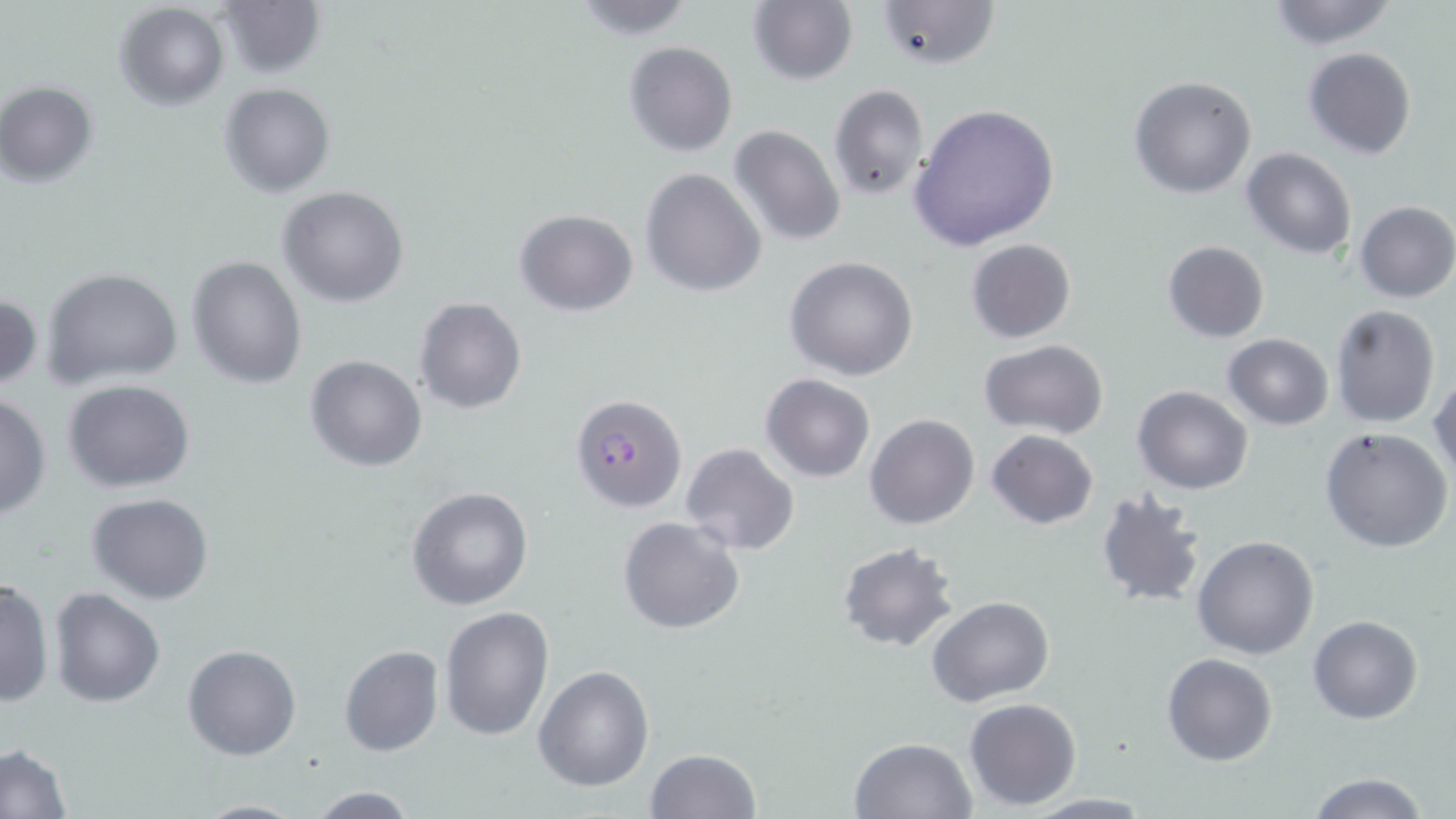

Summary:
  - Coordinate format: approximate bounding boxes as [x1, y1, x2, y2] in pixels
  - Plasmodium falciparum-infected red blood cell locations: [570, 393, 687, 514]
  - Uninfected red blood cell locations: [566, 0, 699, 40], [748, 0, 858, 85], [872, 0, 998, 70], [1261, 0, 1401, 50], [215, 2, 324, 78], [114, 3, 229, 111], [623, 41, 738, 157], [1301, 47, 1417, 160], [1129, 74, 1258, 198], [1, 80, 98, 186], [219, 82, 336, 198], [828, 84, 930, 201], [907, 103, 1061, 251], [728, 125, 847, 247], [1241, 147, 1357, 259], [640, 168, 766, 297], [277, 185, 409, 308], [1355, 200, 1455, 302], [514, 209, 638, 314], [966, 238, 1076, 343], [1162, 240, 1270, 342], [785, 255, 918, 380], [187, 256, 307, 390], [40, 267, 187, 394], [0, 291, 43, 392], [414, 297, 526, 414], [1329, 303, 1441, 428], [1221, 333, 1335, 431], [979, 340, 1108, 439], [304, 354, 428, 471], [761, 373, 875, 483], [1430, 373, 1456, 485], [63, 380, 196, 493], [1133, 384, 1253, 494], [0, 391, 51, 521], [864, 413, 979, 530], [1320, 425, 1454, 553], [986, 430, 1097, 528], [680, 443, 798, 554], [406, 487, 533, 611], [1093, 490, 1207, 609], [87, 493, 215, 605], [618, 516, 746, 636], [1192, 534, 1320, 660], [838, 542, 960, 653], [0, 576, 54, 707], [49, 588, 165, 707], [927, 596, 1054, 707], [439, 606, 554, 742], [1308, 614, 1424, 724], [182, 644, 301, 761], [339, 645, 444, 757], [1162, 653, 1278, 767], [533, 665, 653, 791], [964, 697, 1080, 809], [849, 736, 979, 819], [0, 744, 73, 819], [645, 747, 761, 818], [1303, 773, 1433, 819], [303, 785, 425, 818], [1020, 793, 1157, 817], [188, 798, 309, 818]
  - Slide-level diagnosis: Plasmodium falciparum
  - Modality: optical microscopy
  - Image size: 1456×819 pixels
  - Stain: May-Grünwald-Giemsa
  - Magnification: 1000x
  - Preparation: thin blood film
  - Field of view: single